Assess this cell for malaria.
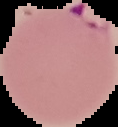

Parasitized.

image size = 118×127 pixels
image type = cell region segmented out of the field of view; surrounding area masked to black
preparation = thin blood smear